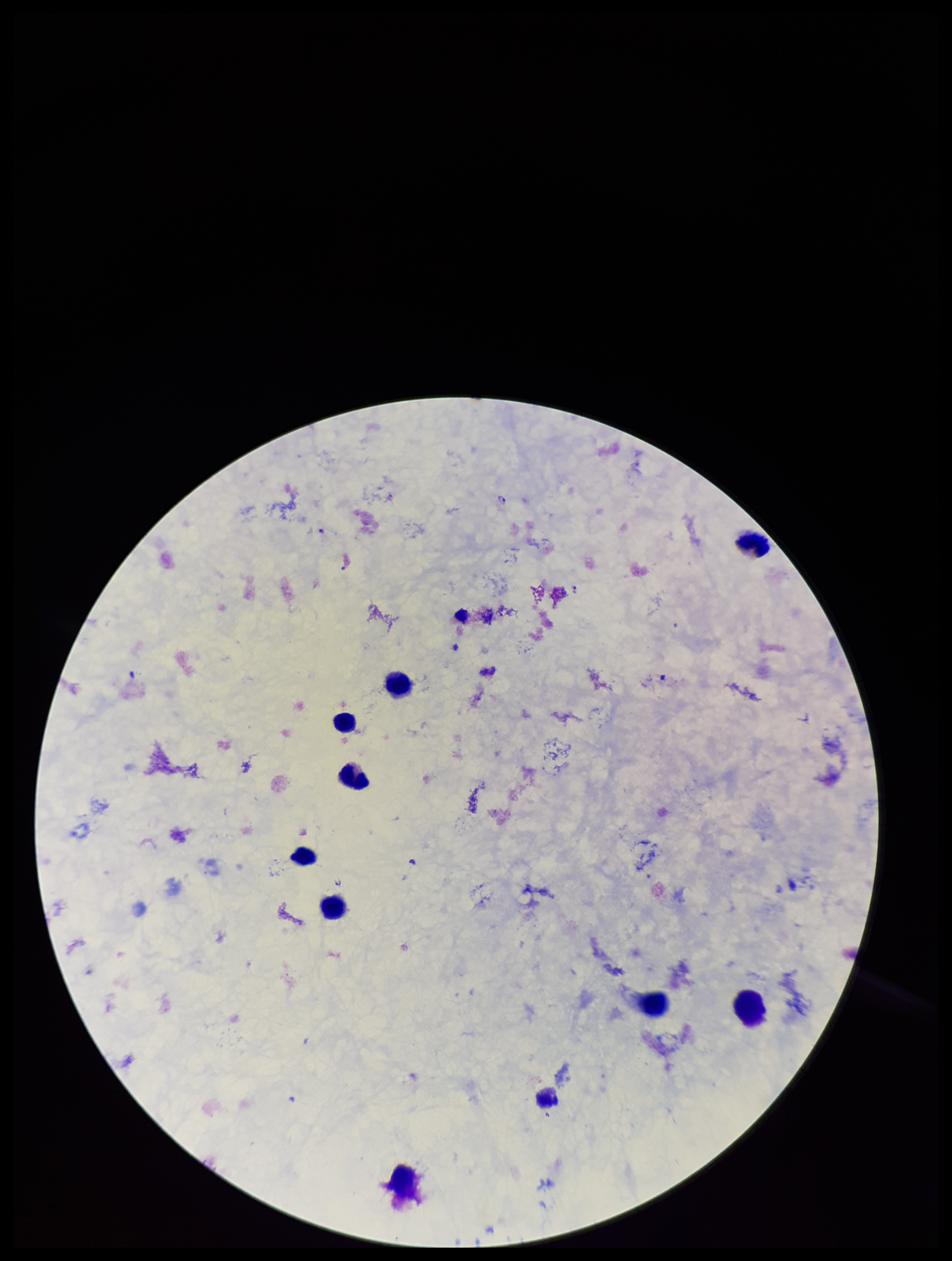

{
  "patient_malaria_status": "infected",
  "leukocyte_count": 10,
  "stain": "Giemsa",
  "field_of_view": "single",
  "preparation": "thick blood smear",
  "species_reported_for_this_patient": "Plasmodium falciparum",
  "image_size": "952×1261 pixels",
  "capture": "smartphone photograph through the microscope eyepiece",
  "plasmodium_parasites": "identified",
  "parasite_count": 1
}